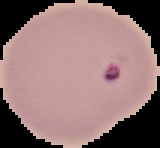

Summary:
  - Preparation: thin blood smear
  - Result: malaria parasites identified
  - Image type: cell region segmented out of the field of view; surrounding area masked to black
  - Image size: 160×148 pixels